State the blood parasite species.
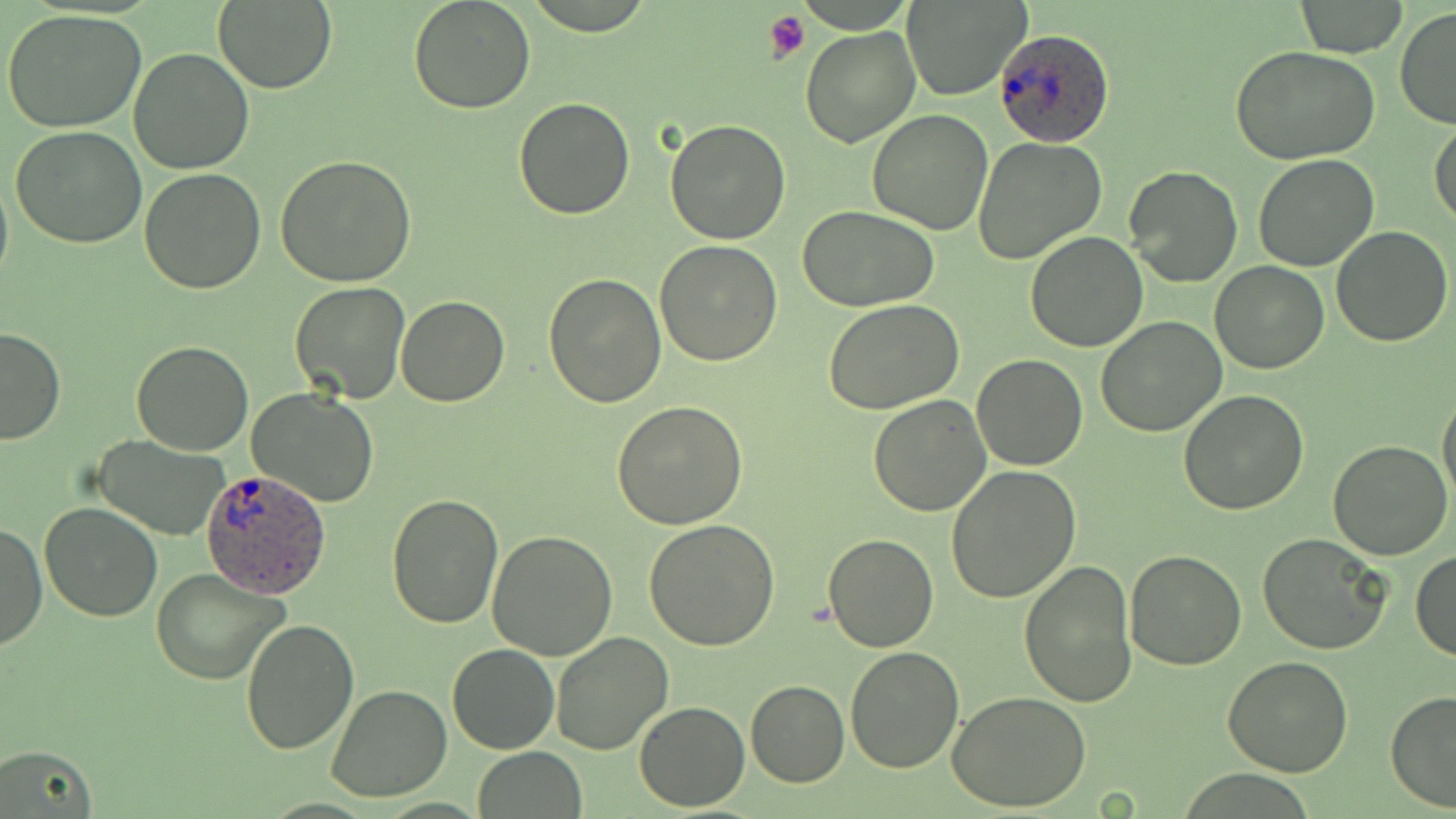
Plasmodium ovale.

modality = optical microscopy
preparation = thin blood film
field of view = single
magnification = 1000x
platelet locations = approximate bounding boxes as (x1, y1, x2, y2) in pixels: (765, 10, 811, 62)
stain = May-Grünwald-Giemsa
uninfected red blood cell locations = approximate bounding boxes as (x1, y1, x2, y2) in pixels: (407, 0, 536, 114), (904, 0, 1027, 100), (212, 1, 337, 92), (1295, 1, 1407, 57), (1395, 7, 1456, 130), (3, 9, 150, 133), (800, 27, 922, 148), (1232, 47, 1381, 165), (129, 48, 254, 173), (514, 99, 636, 220), (867, 110, 993, 236), (1430, 117, 1456, 229), (663, 119, 791, 245), (10, 125, 148, 249), (974, 137, 1106, 265), (277, 154, 418, 285), (1253, 156, 1379, 272), (1123, 166, 1242, 287), (140, 168, 268, 295), (0, 170, 12, 292), (798, 205, 940, 312), (1331, 227, 1453, 347), (1024, 230, 1148, 352), (655, 240, 783, 367), (1209, 259, 1329, 374), (544, 272, 667, 408), (289, 281, 413, 404), (395, 295, 510, 406), (822, 298, 965, 414), (1096, 317, 1227, 438), (0, 326, 66, 446), (131, 340, 254, 455), (972, 355, 1088, 472), (249, 387, 379, 508), (1178, 390, 1311, 515), (1438, 392, 1456, 508), (868, 395, 992, 516), (612, 401, 748, 530), (92, 436, 231, 540), (1328, 440, 1453, 560), (947, 463, 1080, 603), (386, 495, 505, 628), (41, 503, 162, 622), (646, 520, 781, 649), (1, 521, 46, 652), (486, 530, 619, 662), (1257, 533, 1391, 653), (823, 534, 939, 652), (1124, 549, 1246, 671), (1412, 550, 1456, 660), (1020, 560, 1138, 707), (151, 567, 290, 684), (239, 619, 360, 755), (550, 632, 674, 755), (447, 642, 559, 754), (844, 646, 964, 774), (1223, 656, 1353, 775), (746, 679, 850, 787), (329, 684, 452, 802), (1386, 690, 1456, 813), (948, 691, 1094, 812), (634, 701, 750, 812), (0, 745, 98, 817), (472, 748, 587, 819)
image size = 1456×819 pixels
Plasmodium ovale-infected red blood cell locations = approximate bounding boxes as (x1, y1, x2, y2) in pixels: (994, 29, 1118, 148), (199, 470, 331, 595)